Assess the morphology of the erythrocytes.
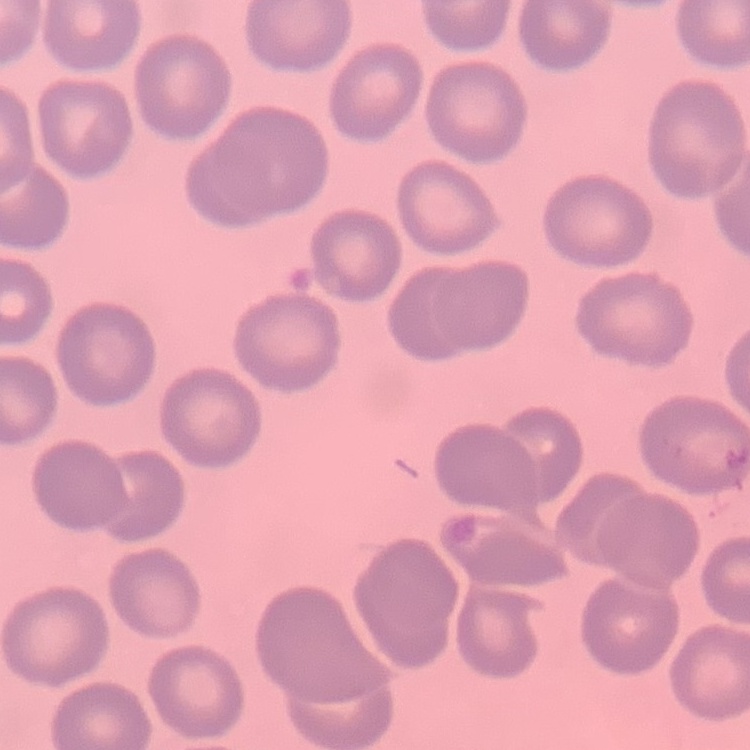

No rouleaux formation.

One tile cut from a larger photomicrograph. Thin blood smear. Field's or Giemsa stain.